Give the extent of all uninfected red blood cells.
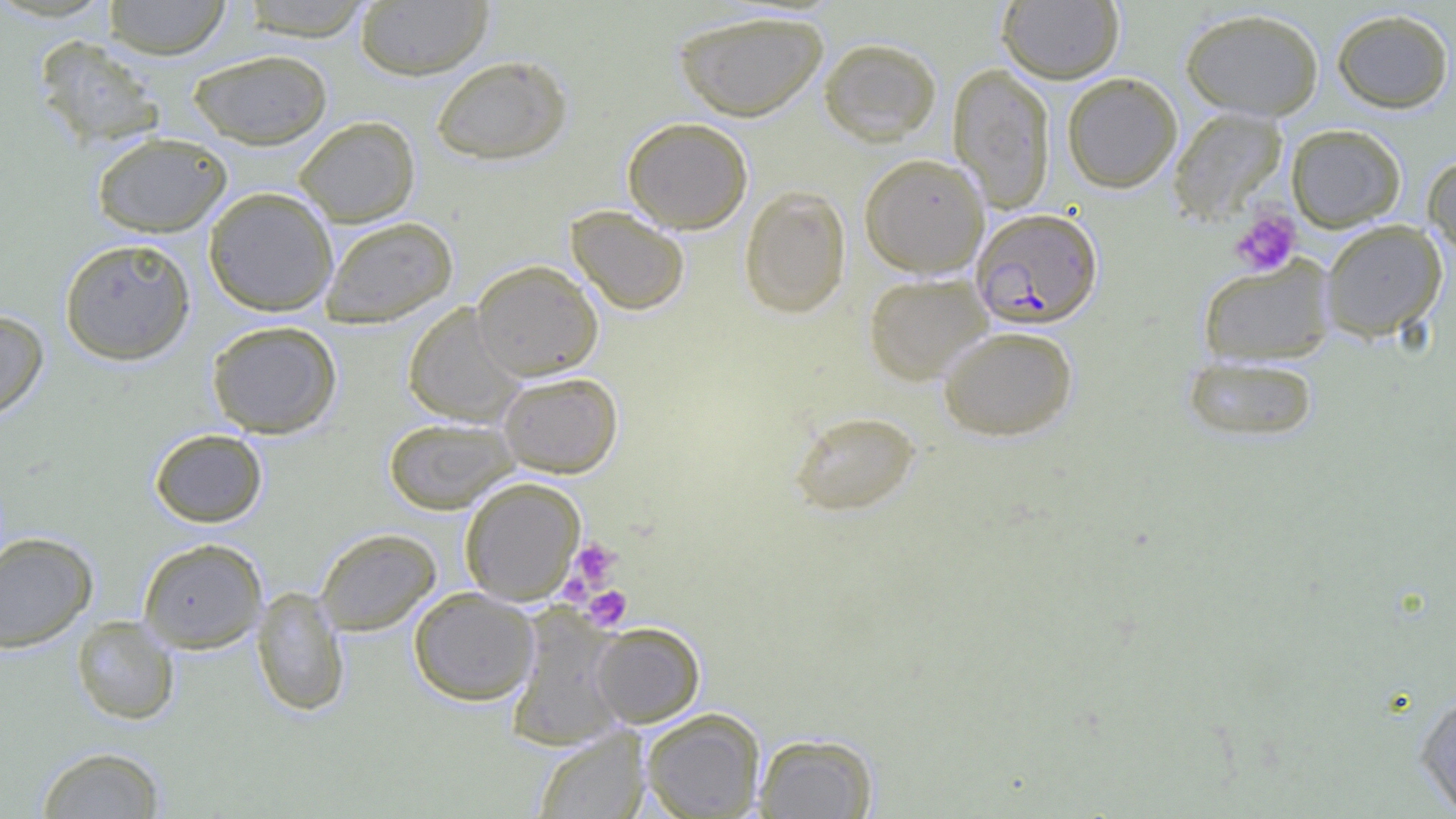
Approximate bounding boxes as [x1, y1, x2, y2] in pixels.
Uninfected red blood cells: [103, 0, 232, 59], [238, 0, 378, 40], [997, 0, 1123, 84], [355, 1, 493, 81], [1180, 7, 1324, 121], [1331, 8, 1455, 113], [672, 9, 829, 122], [33, 35, 167, 150], [818, 37, 942, 146], [187, 48, 334, 149], [431, 54, 572, 165], [948, 63, 1056, 213], [1062, 72, 1182, 193], [1167, 107, 1287, 226], [293, 116, 420, 227], [622, 117, 753, 234], [1286, 124, 1406, 232], [91, 131, 232, 238], [859, 153, 989, 278], [1423, 154, 1456, 259], [739, 184, 851, 318], [204, 187, 339, 316], [565, 204, 691, 316], [321, 216, 458, 328], [1320, 220, 1448, 342], [59, 237, 197, 366], [1197, 256, 1337, 367], [471, 259, 604, 380], [863, 273, 993, 386], [402, 304, 526, 426], [0, 309, 49, 423], [206, 320, 342, 438], [937, 324, 1078, 442], [1182, 353, 1320, 443], [498, 371, 623, 477], [788, 410, 921, 517], [383, 416, 519, 514], [149, 428, 268, 528], [459, 476, 585, 605], [315, 528, 441, 635], [0, 531, 99, 652], [138, 538, 267, 653], [252, 587, 351, 716], [408, 588, 539, 706], [506, 609, 626, 750], [71, 615, 180, 725], [592, 622, 705, 727], [1414, 687, 1456, 816], [641, 708, 766, 818], [532, 727, 650, 818], [754, 733, 878, 818], [35, 746, 166, 818].

Plasmodium falciparum-infected red blood cell locations: [971, 208, 1104, 329]. Platelet locations: [1230, 207, 1301, 277], [565, 538, 622, 595], [582, 585, 633, 631]. Slide-level diagnosis: Plasmodium falciparum. Image is 1456×819 pixels. Thin blood film. 1000x magnification. Light microscopy. One field of a larger specimen.